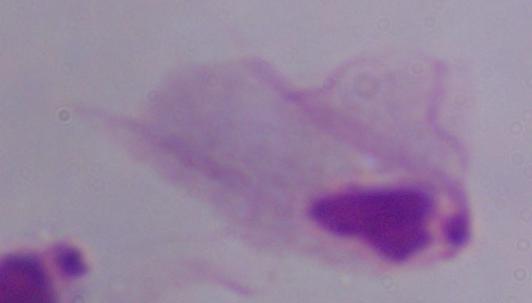

magnification = 1000x
identification = trichomonad
modality = photomicrograph